Name the blood parasite species.
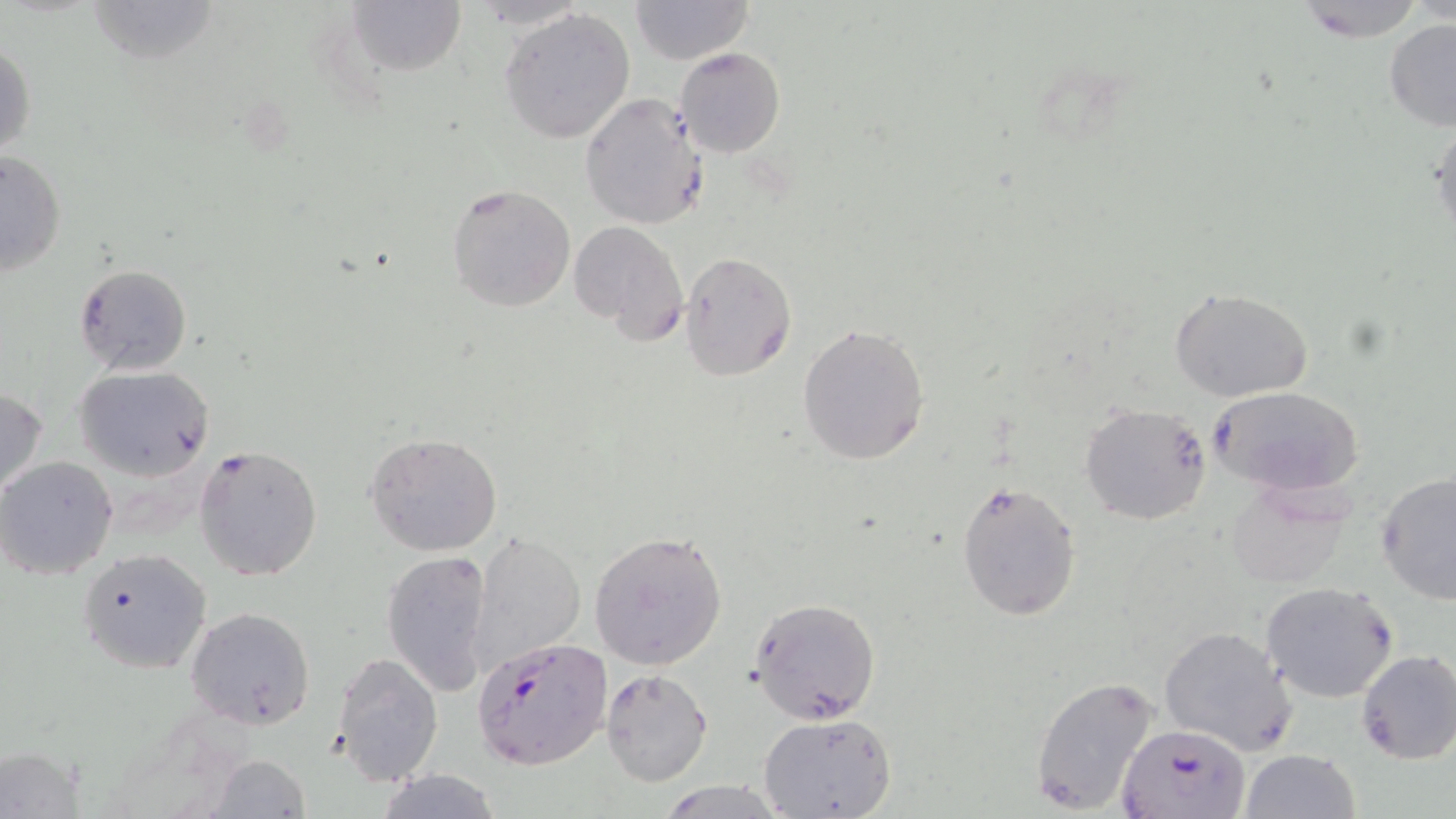

Plasmodium falciparum.

magnification = 1000x
Plasmodium falciparum-infected red blood cell locations = approximate bounding boxes as (x1, y1, x2, y2) in pixels: (472, 635, 611, 769), (1117, 722, 1249, 819)
field of view = single
preparation = thin blood smear
stain = May-Grünwald-Giemsa
image size = 1456×819 pixels
modality = optical microscopy
uninfected red blood cell locations = approximate bounding boxes as (x1, y1, x2, y2) in pixels: (85, 0, 221, 68), (347, 0, 466, 78), (469, 0, 589, 28), (629, 0, 756, 65), (1293, 0, 1431, 42), (499, 7, 637, 144), (1384, 18, 1456, 131), (1, 37, 35, 163), (675, 46, 785, 157), (579, 92, 709, 229), (1428, 110, 1456, 243), (1, 150, 67, 277), (446, 183, 577, 312), (570, 221, 688, 343), (679, 252, 796, 379), (73, 263, 191, 377), (1171, 288, 1315, 402), (797, 325, 930, 466), (74, 365, 214, 480), (1210, 385, 1365, 497), (0, 386, 49, 502), (1080, 403, 1211, 525), (364, 431, 505, 558), (194, 443, 324, 582), (0, 457, 118, 580), (1376, 471, 1456, 605), (955, 480, 1082, 622), (1225, 481, 1353, 590), (589, 529, 728, 672), (470, 532, 587, 674), (77, 547, 212, 675), (382, 549, 493, 698), (1262, 580, 1398, 703), (749, 597, 882, 723), (185, 606, 316, 730), (1158, 627, 1296, 755), (1357, 648, 1456, 765), (330, 652, 444, 787), (602, 669, 714, 787), (1028, 673, 1163, 818), (758, 713, 897, 819), (0, 744, 87, 819), (1242, 748, 1359, 819), (205, 755, 312, 818), (375, 768, 504, 819), (659, 781, 785, 817)